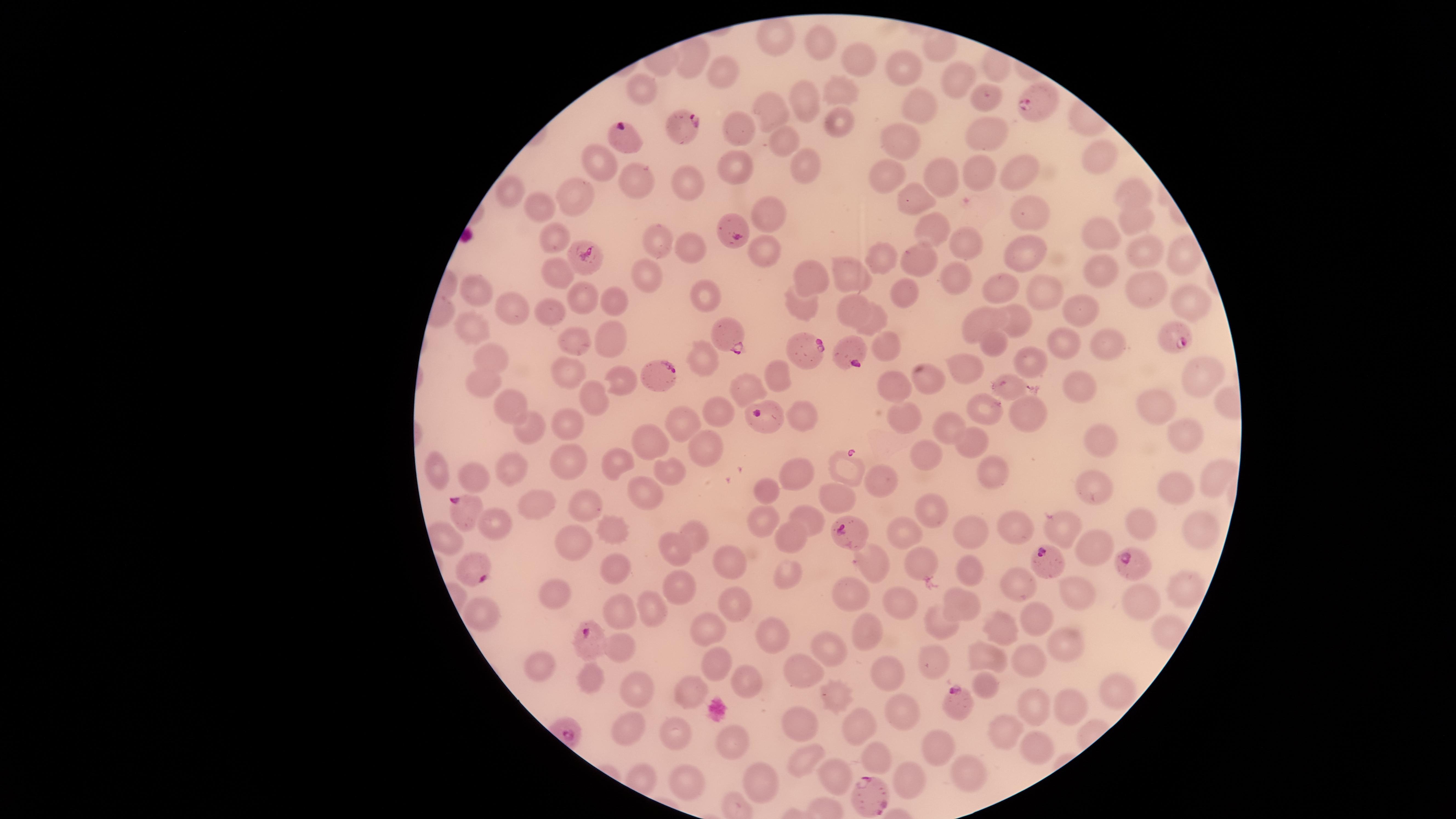
capture: smartphone photograph through the microscope eyepiece
uninfected_RBCs: 'approximate marker points as {x, y} in pixels: {773, 38}, {817, 40}, {861, 59}, {694, 62}, {902, 63}, {730, 71}, {957, 75}, {644, 90}, {841, 92}, {805, 99}, {986, 100}, {919, 102}, {767, 110}, {838, 116}, {741, 129}, {986, 133}, {787, 139}, {904, 140}, {600, 160}, {804, 162}, {1100, 163}, {738, 164}, {1017, 170}, {939, 172}, {977, 175}, {889, 176}, {683, 179}, {641, 181}, {509, 188}, {569, 193}, {1136, 196}, {915, 197}, {543, 206}, {768, 211}, {1029, 213}, {1137, 220}, {931, 227}, {1103, 234}, {554, 240}, {662, 242}, {966, 242}, {690, 249}, {1024, 250}, {1146, 250}, {1183, 254}, {761, 257}, {883, 258}, {918, 258}, {851, 272}, {558, 273}, {646, 275}, {1102, 277}, {808, 278}, {957, 278}, {1001, 288}, {475, 289}, {905, 290}, {1041, 291}, {584, 294}, {704, 294}, {1144, 294}, {610, 298}, {1187, 298}, {801, 304}, {512, 307}, {847, 307}, {552, 312}, {1017, 317}, {1084, 317}, {979, 318}, {876, 320}, {473, 326}, {610, 336}, {887, 342}, {991, 342}, {572, 343}, {1117, 343}, {1063, 344}, {488, 354}, {701, 357}, {1034, 361}, {965, 366}, {569, 371}, {1200, 371}, {783, 375}, {618, 377}, {929, 379}, {485, 383}, {749, 384}, {893, 385}, {1010, 387}, {1079, 392}, {592, 397}, {508, 400}, {719, 405}, {1156, 406}, {983, 408}, {900, 411}, {1029, 412}, {802, 415}, {569, 418}, {685, 419}, {943, 425}, {531, 426}, {1182, 434}, {1102, 436}, {971, 440}, {649, 441}, {711, 443}, {927, 452}, {435, 463}, {566, 463}, {616, 464}, {846, 465}, {513, 466}, {673, 468}, {995, 470}, {799, 473}, {473, 475}, {1216, 476}, {881, 481}, {1174, 484}, {765, 490}, {1096, 490}, {642, 493}, {836, 495}, {586, 500}, {541, 506}, {933, 511}, {763, 517}, {807, 519}, {1019, 523}, {495, 524}, {617, 524}, {1197, 525}, {1065, 527}, {1144, 529}, {971, 530}, {905, 531}, {691, 533}, {793, 537}, {448, 541}, {570, 542}, {1093, 550}, {673, 554}, {915, 559}, {876, 563}, {732, 564}, {613, 568}, {962, 569}, {786, 574}, {1015, 582}, {1179, 584}, {851, 590}, {676, 592}, {551, 595}, {1074, 598}, {897, 602}, {1142, 602}, {960, 603}, {731, 605}, {481, 609}, {615, 609}, {656, 609}, {1038, 618}, {945, 620}, {708, 630}, {772, 632}, {1002, 632}, {871, 633}, {1061, 643}, {826, 644}, {621, 648}, {989, 657}, {1026, 659}, {934, 660}, {543, 661}, {714, 662}, {888, 666}, {799, 669}, {739, 679}, {591, 681}, {986, 681}, {634, 683}, {1114, 689}, {838, 692}, {692, 694}, {1028, 703}, {1071, 704}, {902, 712}, {802, 720}, {857, 723}, {625, 726}, {676, 734}, {1002, 734}, {728, 743}, {946, 748}, {1039, 751}, {808, 753}, {877, 756}, {759, 772}, {841, 774}, {982, 778}, {910, 779}, {695, 781}'
image_size: 1456×819 pixels
species: Plasmodium falciparum
visible_region: circular
field_of_view: single
preparation: thin blood smear
parasitized_RBCs: 'approximate marker points as {x, y} in pixels: {1032, 101}, {682, 124}, {621, 138}, {735, 230}, {583, 261}, {1175, 336}, {725, 338}, {851, 352}, {808, 353}, {662, 376}, {763, 412}, {462, 506}, {852, 534}, {1041, 557}, {473, 569}, {1133, 569}, {591, 635}, {954, 697}, {867, 785}'
presence: malaria parasites identified
stain: Giemsa